Give the position of every malaria parasite and every leukocyte.
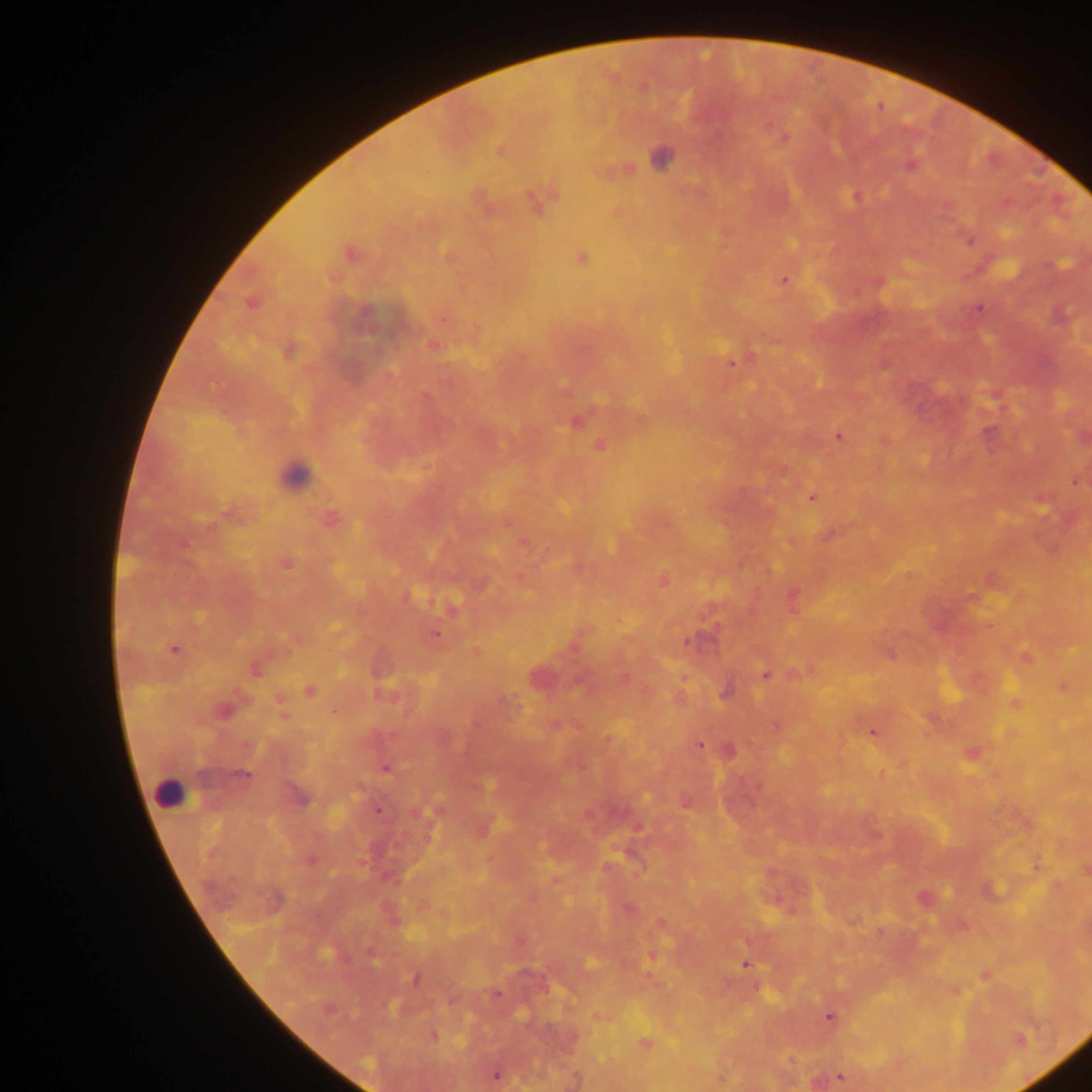
Approximate centers as {x, y} in pixels.
Malaria parasites: {785, 137}, {501, 151}, {911, 165}, {855, 197}, {537, 201}, {616, 212}, {970, 240}, {351, 254}, {581, 258}, {784, 280}, {879, 281}, {251, 303}, {978, 308}, {732, 362}, {425, 397}, {575, 423}, {839, 437}, {600, 445}, {1076, 481}, {812, 498}, {329, 520}, {286, 564}, {663, 580}, {435, 635}, {686, 641}, {174, 649}, {889, 654}, {1027, 658}, {256, 669}, {764, 675}, {624, 678}, {1064, 688}, {310, 691}, {725, 693}, {1015, 702}, {223, 710}, {335, 712}, {775, 726}, {872, 732}, {699, 745}, {386, 769}, {243, 774}, {378, 811}, {309, 860}, {628, 908}, {660, 925}, {373, 956}, {591, 963}, {746, 964}, {415, 979}, {495, 995}, {830, 1017}, {434, 1037}, {1019, 1040}, {645, 1043}, {496, 1075}, {840, 1078}.
Leukocytes: {295, 475}, {169, 792}.
One object is labeled both malaria parasite and leukocyte by the source: {659, 159}.

Thick blood film. Mobile-phone photograph taken through the microscope. Collected in Ghana. Single field of view. Image is 1092×1092 pixels.